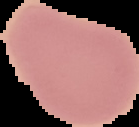
image type = cell region segmented out of the field of view; surrounding area masked to black
image size = 139×127 pixels
preparation = thin blood smear
result = no Plasmodium parasites detected